Name the parasite shown.
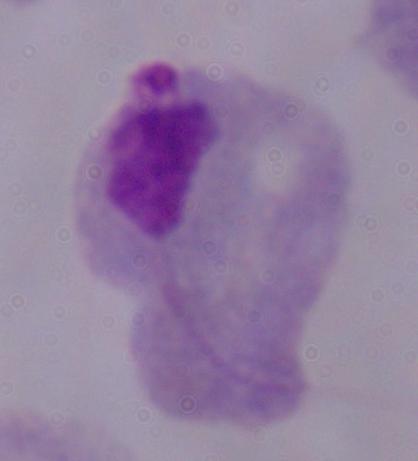

This is a trichomonad.

Summary:
  - Magnification: 1000x
  - Modality: micrograph